Classify this cell by malaria status.
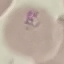
Parasitized.

Automatically extracted cell patch, resized to 64 × 64 pixels. Thin smear of blood. Giemsa-stained preparation. Photographed with a smartphone camera at the microscope eyepiece.